Locate and identify every blood parasite.
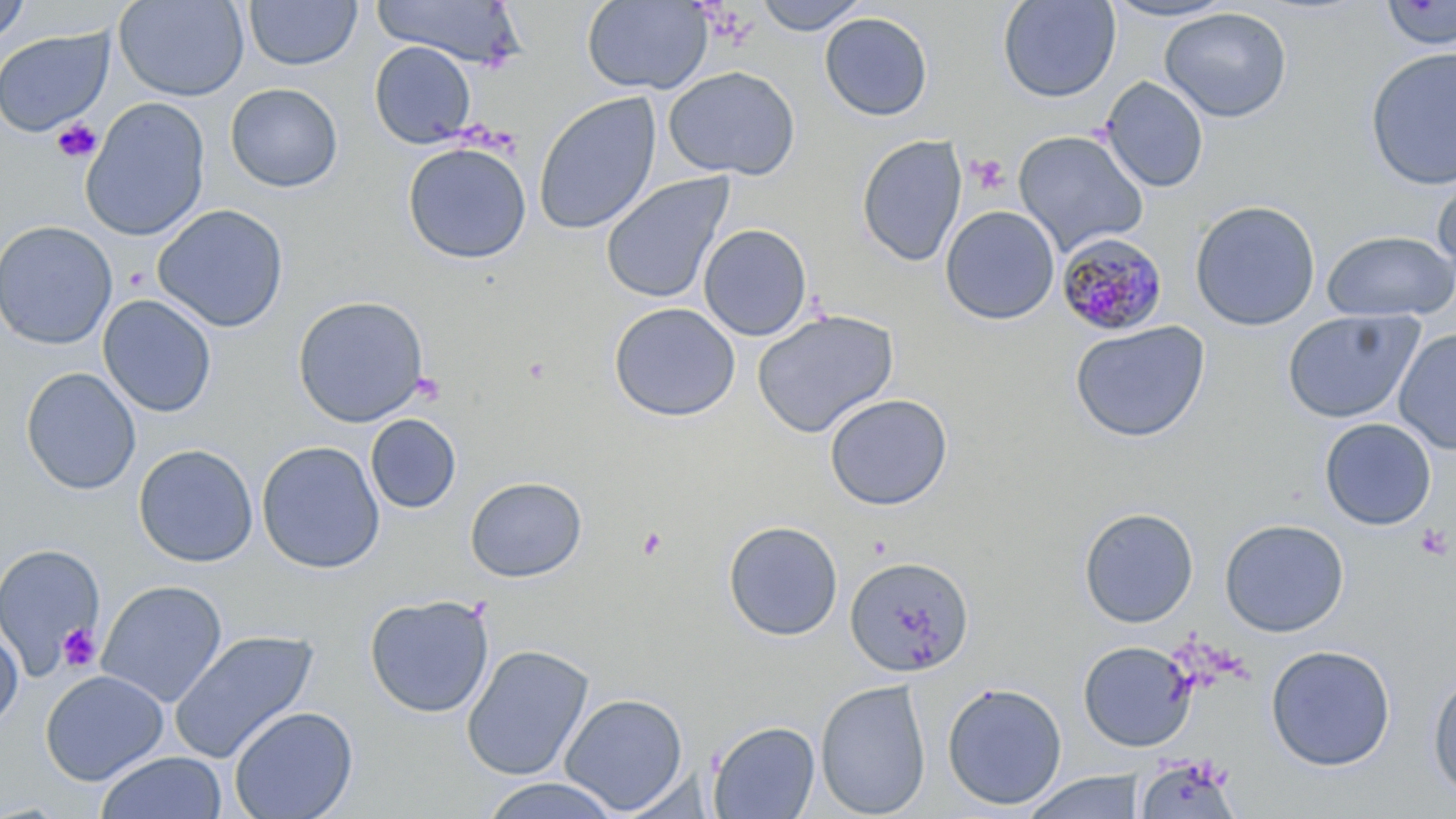
Approximate bounding boxes as [x1, y1, x2, y2] in pixels.
Plasmodium malariae-infected red blood cells: [1056, 232, 1169, 337].
No Plasmodium falciparum, Plasmodium ovale, Plasmodium vivax, Babesia divergens, or Trypanosoma brucei observed.

Uninfected red blood cell locations: [114, 0, 249, 102], [244, 0, 362, 70], [373, 0, 526, 68], [752, 0, 871, 34], [997, 0, 1121, 103], [1100, 0, 1240, 22], [0, 1, 31, 46], [581, 1, 712, 95], [1379, 1, 1456, 51], [1159, 7, 1292, 123], [819, 11, 933, 122], [0, 27, 114, 137], [369, 41, 477, 148], [1365, 47, 1456, 191], [662, 65, 801, 181], [1100, 76, 1209, 193], [225, 82, 343, 193], [533, 91, 662, 236], [80, 97, 210, 241], [1012, 129, 1149, 257], [857, 134, 967, 267], [402, 141, 532, 264], [1430, 170, 1456, 282], [600, 173, 735, 305], [1189, 199, 1321, 332], [152, 203, 289, 333], [940, 205, 1060, 325], [0, 220, 117, 349], [698, 223, 813, 341], [1322, 230, 1456, 322], [97, 294, 217, 418], [292, 295, 430, 428], [608, 302, 741, 422], [752, 309, 899, 439], [1282, 309, 1423, 424], [1070, 321, 1210, 443], [1393, 329, 1456, 454], [21, 366, 141, 495], [824, 393, 953, 511], [365, 414, 462, 514], [1319, 418, 1437, 530], [256, 440, 385, 574], [133, 443, 258, 568], [465, 476, 587, 583], [1079, 507, 1199, 628], [1219, 517, 1350, 637], [723, 519, 843, 641], [0, 542, 106, 680], [844, 554, 974, 678], [96, 580, 228, 707], [363, 593, 495, 718], [0, 623, 24, 733], [169, 629, 319, 764], [1078, 640, 1195, 751], [461, 644, 594, 782], [1265, 644, 1396, 771], [39, 670, 169, 785], [1427, 671, 1456, 800], [815, 679, 931, 818], [941, 681, 1067, 811], [559, 693, 689, 814], [228, 705, 358, 819], [708, 720, 821, 818], [95, 751, 227, 819], [1135, 754, 1243, 818], [617, 769, 717, 817], [1022, 771, 1147, 819], [480, 776, 623, 818]. Platelet locations: [51, 118, 102, 163], [966, 154, 1009, 195], [1414, 522, 1452, 561], [637, 527, 668, 561], [56, 623, 100, 672]. Slide-level diagnosis: Plasmodium malariae. One field of a larger specimen. Optical microscopy. Image is 1456×819 pixels. May-Grünwald-Giemsa stain. Thin blood film. Captured at 1000x magnification.